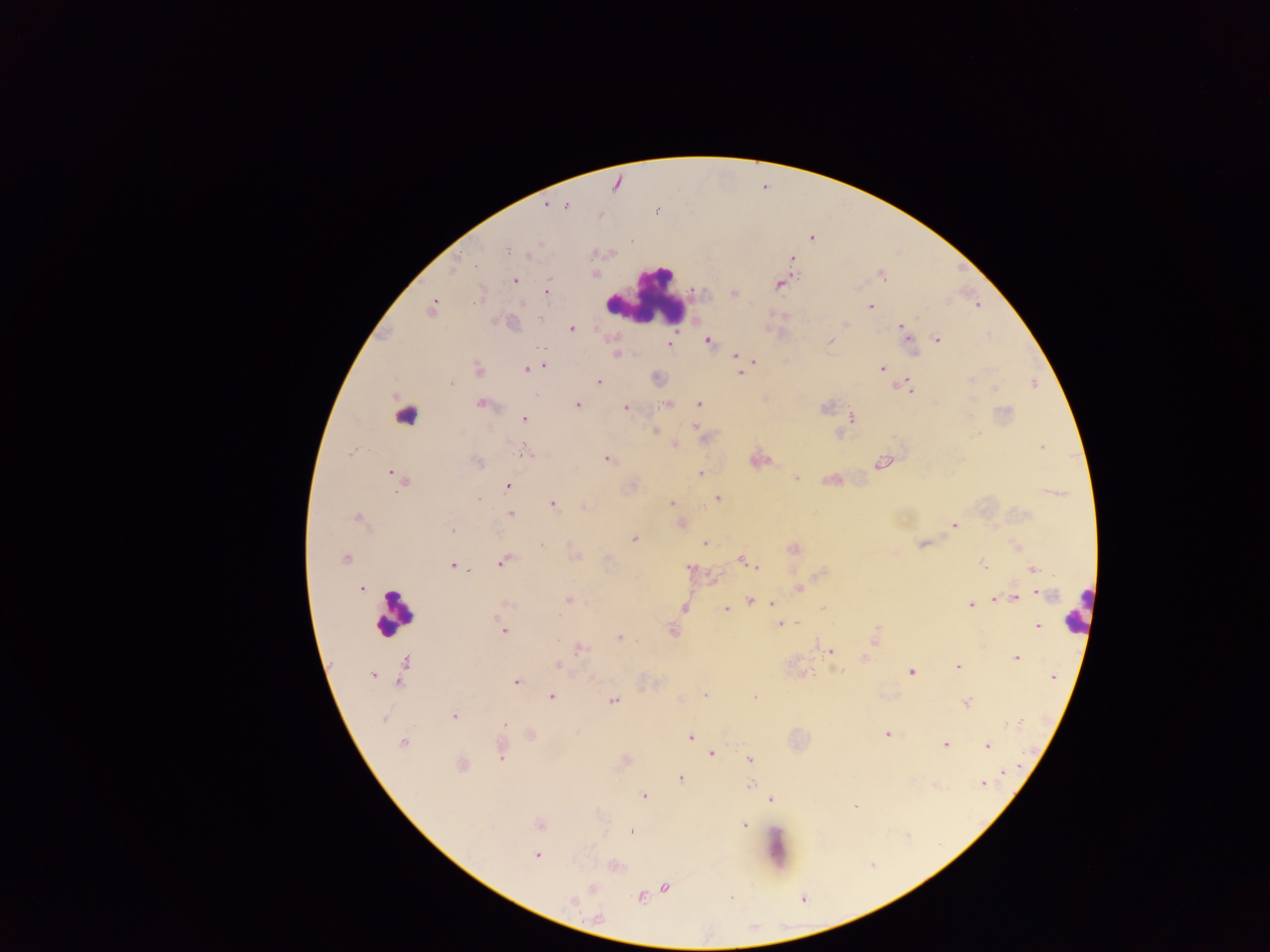
Approximate centers as {x, y} in pixels.
Summary:
  - Leukocyte locations: {647, 294}, {405, 416}, {1078, 610}, {393, 614}, {776, 848}
  - Malaria parasite locations: {616, 183}, {545, 205}, {567, 206}, {600, 215}, {812, 237}, {630, 241}, {506, 248}, {528, 256}, {790, 258}, {454, 269}, {595, 274}, {882, 275}, {513, 279}, {779, 283}, {546, 291}, {734, 294}, {978, 305}, {870, 306}, {432, 308}, {845, 323}, {572, 329}, {902, 329}, {937, 339}, {708, 340}, {829, 341}, {669, 344}, {913, 352}, {616, 353}, {735, 355}, {752, 359}, {786, 360}, {544, 365}, {882, 368}, {527, 369}, {478, 370}, {741, 372}, {656, 377}, {971, 379}, {598, 381}, {907, 385}, {994, 389}, {480, 402}, {668, 403}, {577, 405}, {697, 405}, {626, 407}, {971, 416}, {851, 418}, {524, 419}, {695, 426}, {655, 431}, {837, 433}, {673, 444}, {1042, 447}, {524, 452}, {607, 459}, {758, 459}, {477, 462}, {881, 462}, {392, 472}, {700, 472}, {398, 477}, {796, 477}, {832, 479}, {508, 486}, {717, 498}, {670, 502}, {551, 503}, {583, 506}, {510, 514}, {358, 519}, {679, 522}, {954, 525}, {452, 529}, {634, 538}, {704, 542}, {924, 544}, {1016, 546}, {792, 548}, {574, 556}, {345, 559}, {741, 559}, {503, 561}, {757, 565}, {983, 565}, {454, 566}, {690, 567}, {1033, 569}, {711, 578}, {799, 587}, {361, 588}, {1039, 591}, {1014, 597}, {993, 598}, {567, 599}, {750, 600}, {773, 602}, {505, 605}, {971, 605}, {683, 608}, {725, 609}, {779, 624}, {1037, 626}, {503, 630}, {672, 630}, {874, 637}, {620, 638}, {579, 648}, {830, 651}, {863, 658}, {1016, 658}, {405, 662}, {558, 664}, {957, 666}, {840, 670}, {911, 671}, {403, 672}, {801, 674}, {373, 675}, {1052, 676}, {591, 678}, {515, 681}, {705, 694}, {550, 696}, {754, 698}, {613, 700}, {966, 703}, {454, 716}, {384, 719}, {504, 725}, {1005, 725}, {887, 733}, {530, 734}, {691, 736}, {402, 743}, {945, 743}, {987, 746}, {501, 750}, {712, 752}, {750, 759}, {624, 760}, {462, 765}, {1002, 772}, {680, 778}, {983, 783}, {935, 785}, {749, 786}, {643, 795}, {770, 800}, {853, 805}, {540, 824}, {743, 824}, {630, 831}, {536, 855}, {613, 865}, {665, 887}, {592, 889}, {640, 897}, {573, 902}, {597, 918}
  - Field of view: single
  - Image size: 1270×952 pixels
  - Country: Ghana
  - Capture: mobile-phone photograph through a microscope
  - Preparation: thick blood film